State the preparation type.
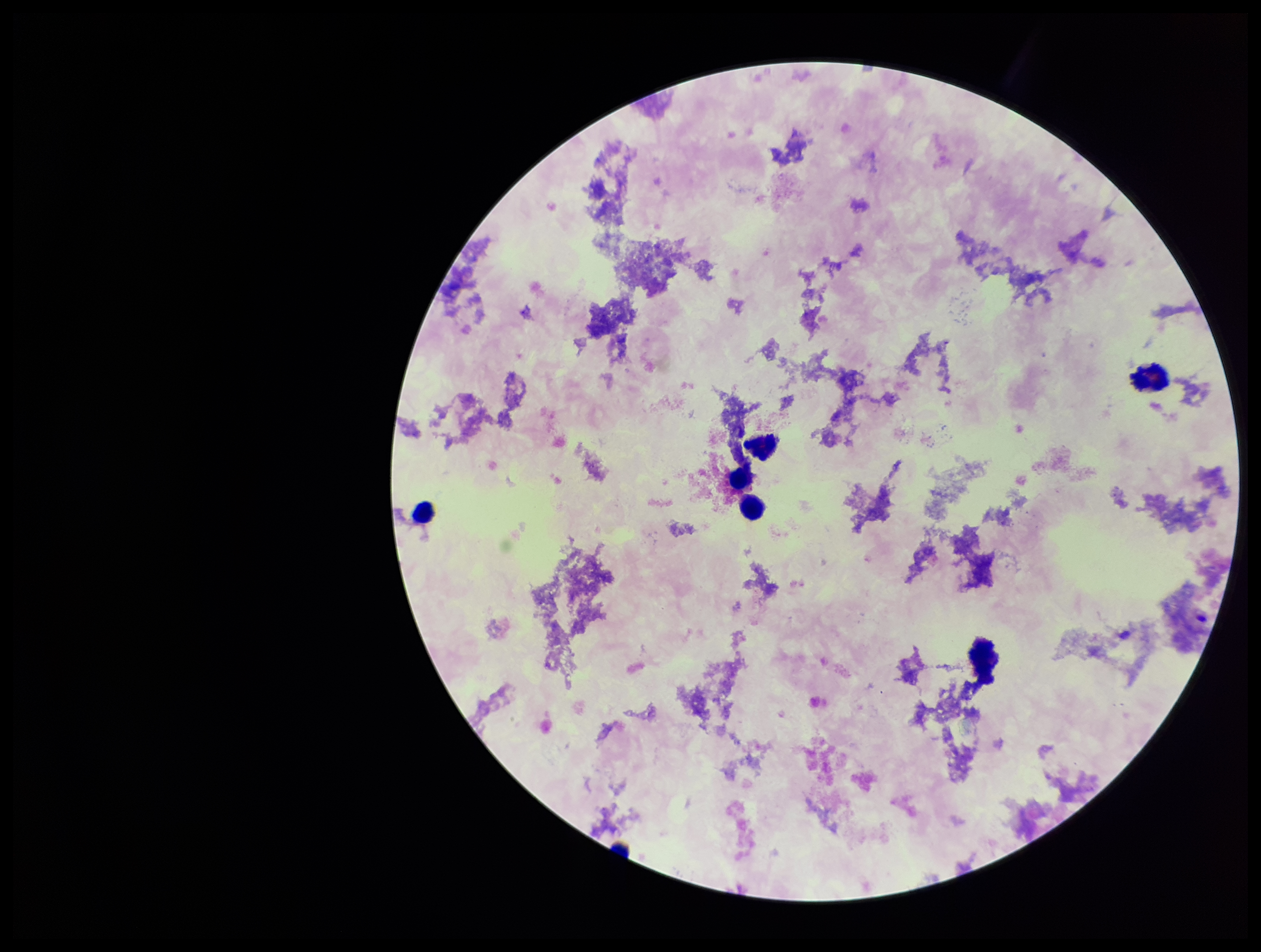

It is a thick blood smear.

patient malaria status = negative
image size = 1261×952 pixels
stain = Giemsa
capture = smartphone photograph through the microscope eyepiece
leukocyte count = 6
parasite count = 0
Plasmodium parasites = none detected
field of view = one from this slide